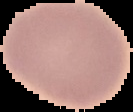

The area outside the segmented cell region is set to black. From a thin blood smear. Malaria status: uninfected. Image is 133×112 pixels.